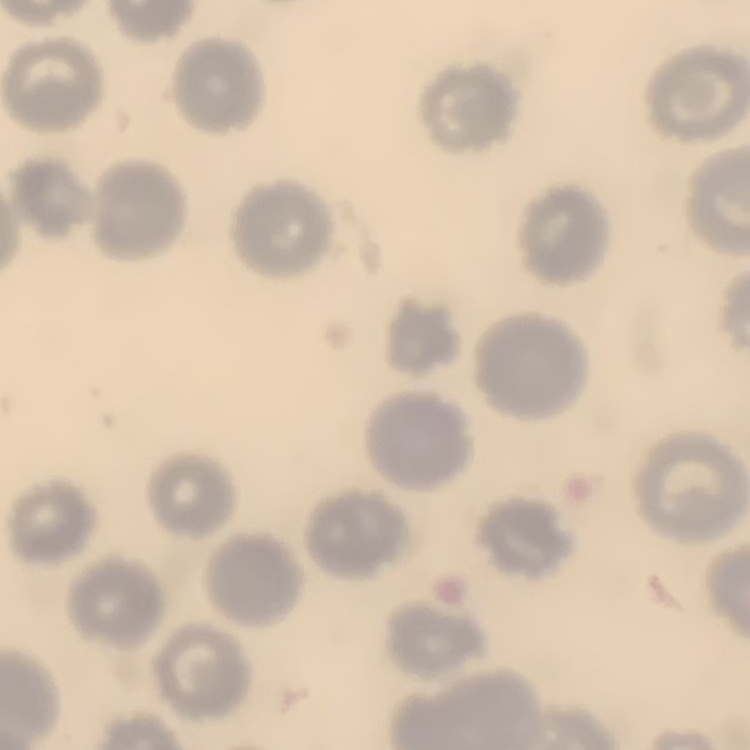

The erythrocytes exhibit no rouleaux formation. Square crop of a larger photomicrograph. Thin blood film. Field's or Giemsa stain.